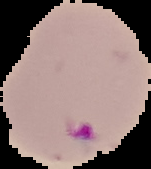
Summary:
  - Image type: segmented cell region with the area outside set to black
  - Malaria status: parasitized
  - Image size: 151×169 pixels
  - Preparation: thin blood film